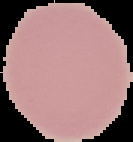

{
  "image_type": "cell region segmented out of the field of view; surrounding area masked to black",
  "image_size": "133×142 pixels",
  "preparation": "thin blood smear",
  "malaria_status": "uninfected"
}